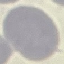

result = no malaria parasites detected
image type = cell patch, automatically extracted from a larger field of view and resized to 64 × 64 pixels
stain = Giemsa
capture = smartphone camera at the microscope eyepiece
preparation = thin blood smear